State which parasite is depicted.
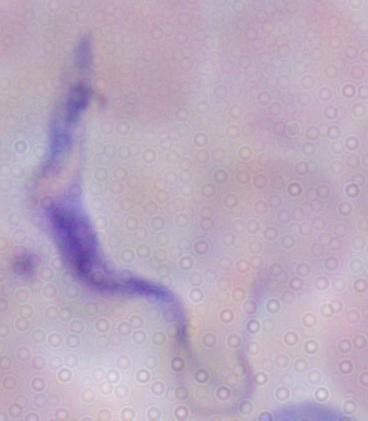
This is a trypanosome.

Summary:
  - Magnification: 1000x
  - Modality: micrograph